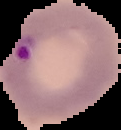
Summary:
  - Image type: segmented cell region with the area outside set to black
  - Image size: 121×130 pixels
  - Malaria status: parasitized
  - Preparation: thin blood smear